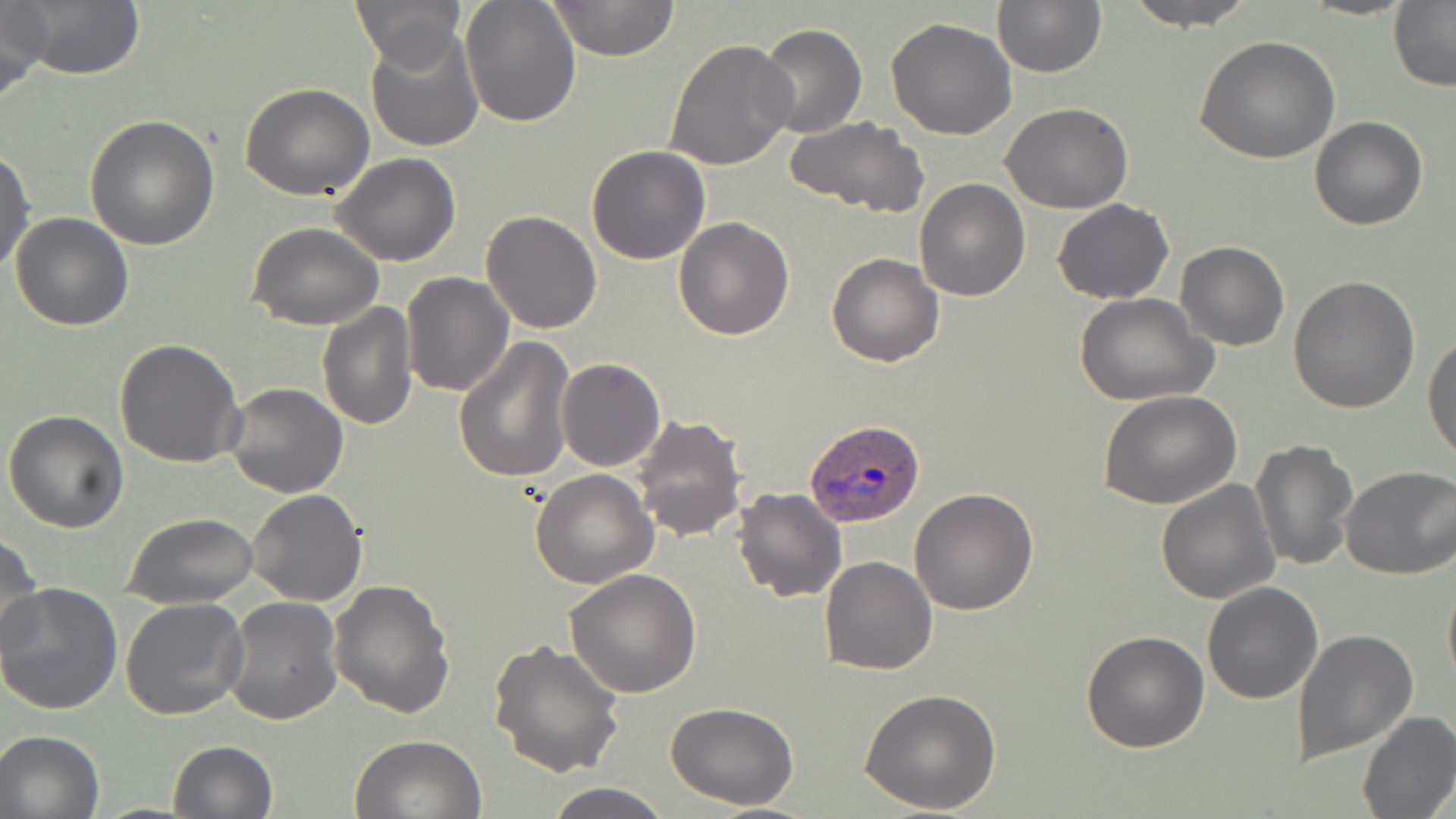
Summary:
  - Coordinate format: approximate bounding boxes as (x1,y1)-(x2,y2) corner pairs in pixels
  - Plasmodium ovale-infected red blood cell locations: (804,417)-(924,525)
  - Uninfected red blood cell locations: (0,0)-(49,103), (12,0)-(146,82), (350,0)-(467,72), (460,0)-(580,126), (546,0)-(679,63), (992,0)-(1106,77), (1121,0)-(1259,29), (1299,0)-(1416,21), (1388,2)-(1456,89), (885,18)-(1018,139), (755,22)-(867,138), (364,26)-(486,152), (1195,35)-(1340,165), (663,38)-(796,171), (241,82)-(374,202), (1002,103)-(1133,214), (85,114)-(221,250), (786,115)-(930,218), (1310,115)-(1428,231), (586,144)-(711,265), (0,148)-(36,278), (330,152)-(461,267), (913,178)-(1032,301), (1052,200)-(1175,304), (480,209)-(601,333), (9,212)-(134,331), (674,216)-(794,339), (247,222)-(385,330), (424,236)-(594,375), (1174,240)-(1289,351), (826,252)-(943,367), (401,272)-(513,397), (1288,274)-(1422,414), (1073,292)-(1219,406), (317,300)-(419,431), (1423,333)-(1456,462), (452,337)-(574,485), (113,338)-(244,469), (556,358)-(666,472), (224,383)-(347,498), (1098,390)-(1244,509), (3,410)-(130,533), (630,413)-(748,543), (1250,439)-(1359,573), (1339,466)-(1456,580), (530,470)-(657,588), (1156,479)-(1281,604), (733,487)-(847,603), (909,487)-(1038,614), (247,489)-(366,607), (122,511)-(258,608), (0,533)-(45,660), (820,555)-(938,675), (564,567)-(701,697), (1442,569)-(1456,692), (329,579)-(457,719), (1202,581)-(1324,703), (0,584)-(124,715), (222,595)-(344,726), (120,597)-(249,721), (1292,628)-(1419,763), (1081,631)-(1209,753), (489,638)-(624,778), (859,688)-(1004,814), (665,701)-(799,811), (1356,710)-(1456,818), (0,729)-(104,818), (350,734)-(486,818), (167,740)-(277,819), (544,780)-(671,818)
  - Slide-level diagnosis: Plasmodium ovale
  - Preparation: thin blood film
  - Modality: light microscopy
  - Magnification: 1000x
  - Field of view: single
  - Image size: 1456×819 pixels
  - Stain: May-Grünwald-Giemsa